Report the malaria status of this cell.
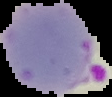

Parasitized.

Summary:
  - Image type: segmented cell region with the area outside set to black
  - Preparation: thin blood film
  - Image size: 112×97 pixels